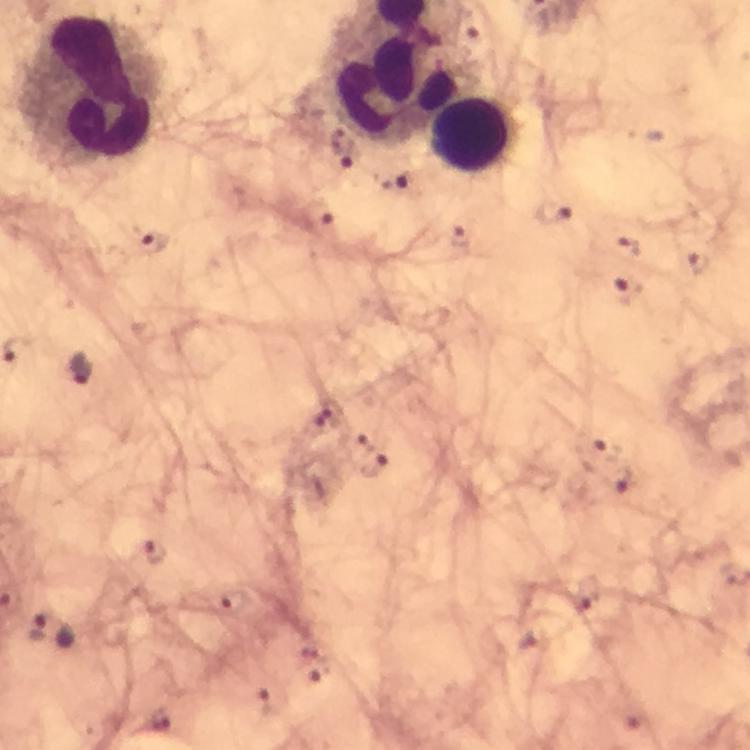 Approximate centers as {x, y} in pixels. Leukocyte locations: {92, 88}, {478, 135}. Malaria parasite locations: {556, 215}, {320, 222}, {459, 238}, {150, 241}, {625, 247}, {631, 293}, {82, 370}, {603, 443}, {373, 465}, {620, 479}, {152, 551}, {39, 627}. Thick smear. A crop from one field of view. At 100x magnification. Immersion oil was used. Giemsa stain. Image is 750×750 pixels. From a malaria diagnostic workup. Photographed through the microscope with a smartphone camera.